Report the malaria status of this cell.
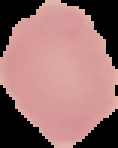

It is uninfected.

image size = 118×148 pixels
image type = segmented cell region with the area outside set to black
preparation = thin blood film